Give the position of every malaria parasite.
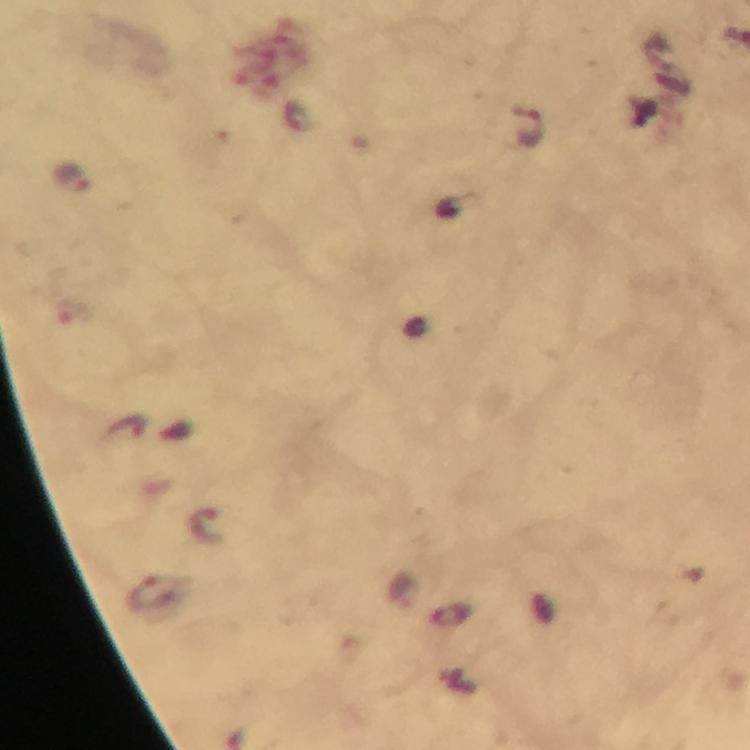
Approximate centers as (x, y) in pixels.
Malaria parasites: (528, 127), (73, 178), (126, 426), (207, 527), (152, 594).

cropped from = a single field of view
immersion oil = applied
stain = Giemsa
preparation = thick blood film
magnification = 100x
capture = smartphone camera through the microscope
context = from a malaria diagnostic workup
image size = 750×750 pixels